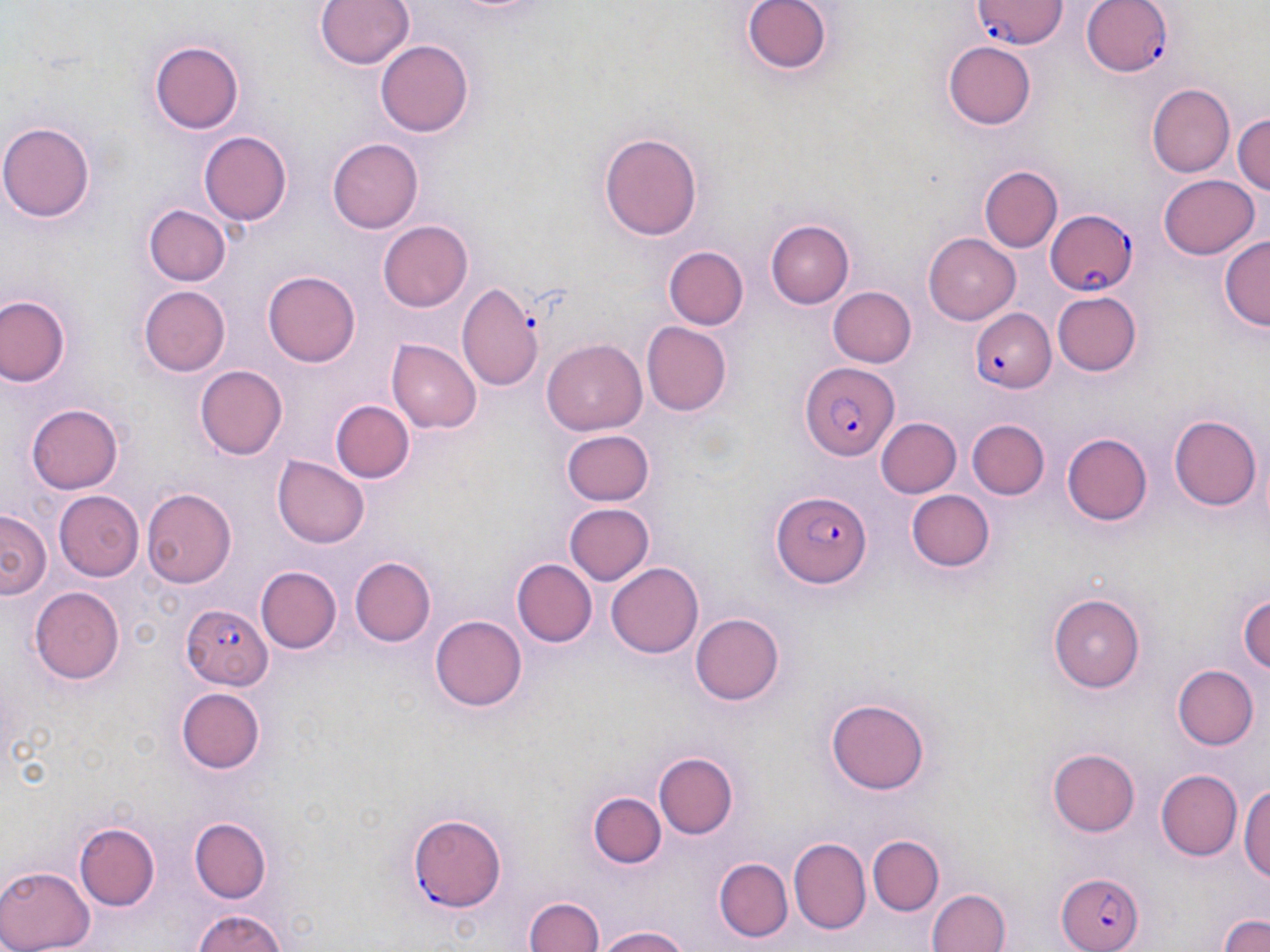
slide-level diagnosis = Plasmodium falciparum
preparation = thin blood smear
stain = May-Grünwald-Giemsa
Plasmodium falciparum-infected red blood cell locations = approximate bounding boxes as (x1, y1, x2, y2) in pixels: (1081, 0, 1171, 79), (969, 1, 1066, 50), (1045, 208, 1137, 295), (967, 308, 1056, 394), (800, 360, 897, 458), (772, 488, 868, 586), (180, 603, 271, 689), (407, 813, 508, 910), (1054, 870, 1145, 952)
field of view = single
image size = 1270×952 pixels
magnification = 1000x
uninfected red blood cell locations = approximate bounding boxes as (x1, y1, x2, y2) in pixels: (317, 0, 415, 71), (740, 0, 833, 78), (150, 38, 245, 135), (376, 39, 471, 136), (944, 41, 1036, 129), (1149, 83, 1235, 177), (1233, 111, 1270, 202), (0, 119, 95, 223), (200, 130, 292, 225), (599, 131, 705, 239), (327, 139, 423, 232), (979, 166, 1062, 251), (1159, 174, 1259, 260), (143, 204, 230, 287), (768, 219, 855, 308), (377, 221, 472, 313), (925, 233, 1019, 323), (1220, 235, 1270, 332), (662, 246, 748, 329), (263, 270, 360, 364), (455, 283, 546, 393), (138, 285, 231, 377), (829, 287, 916, 367), (1052, 293, 1142, 375), (0, 295, 69, 388), (642, 322, 732, 415), (389, 340, 481, 433), (542, 340, 647, 433), (196, 365, 289, 460), (331, 399, 414, 482), (26, 404, 124, 493), (1169, 414, 1260, 511), (967, 417, 1049, 499), (876, 419, 961, 499), (563, 429, 655, 505), (1061, 432, 1152, 526), (274, 456, 368, 547), (905, 488, 994, 573), (142, 489, 237, 588), (55, 491, 143, 581), (565, 503, 655, 586), (1, 509, 49, 602), (510, 556, 599, 646), (349, 558, 434, 647), (608, 561, 703, 659), (255, 565, 340, 654), (30, 587, 126, 684), (1240, 587, 1270, 680), (1053, 590, 1147, 691), (691, 612, 784, 706), (431, 615, 526, 712), (1171, 664, 1259, 751), (173, 686, 266, 775), (826, 696, 932, 795), (1047, 748, 1141, 836), (652, 749, 738, 840), (1155, 769, 1242, 862), (1241, 779, 1270, 889), (588, 790, 663, 870), (186, 815, 277, 905), (72, 817, 161, 914), (869, 836, 942, 916), (788, 839, 871, 933), (714, 857, 793, 943), (0, 863, 95, 952), (927, 888, 1012, 952), (523, 892, 605, 952), (191, 907, 290, 952), (1218, 910, 1270, 952), (593, 926, 696, 952)
modality = light microscopy